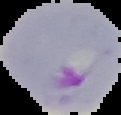
image type = segmented cell region on a black background
preparation = thin blood film
malaria status = parasitized
image size = 121×115 pixels